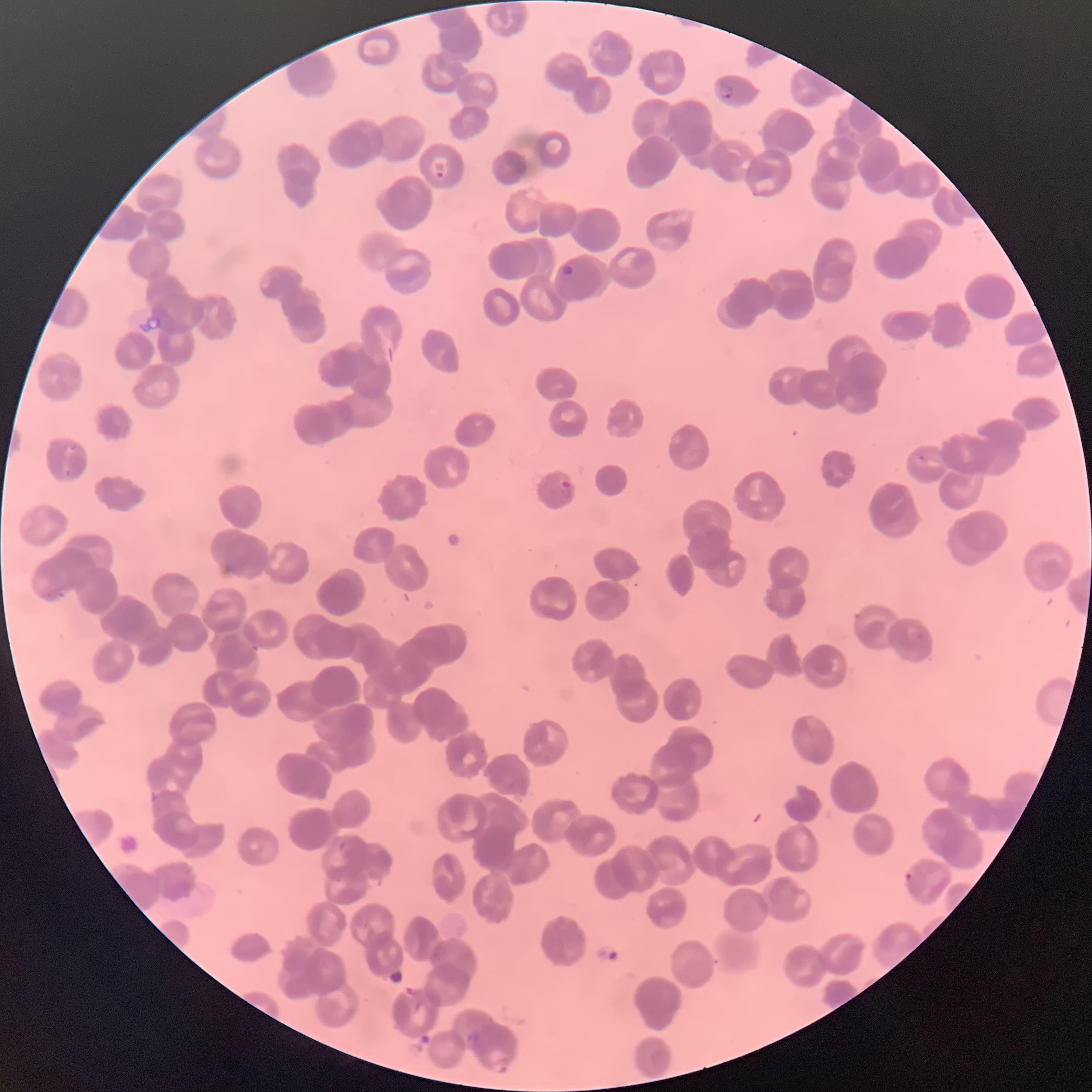
preparation: thin blood film
red_blood_cell_morphology: rouleaux formation
modality: light microscopy
plasmodium_parasite_locations: 'approximate bounding boxes as named x1/y1/x2/y2 corners in pixels: (x1=717, y1=82, x2=734, y2=100), (x1=433, y1=161, x2=446, y2=178), (x1=561, y1=264, x2=574, y2=277), (x1=917, y1=454, x2=926, y2=462), (x1=558, y1=478, x2=572, y2=498), (x1=903, y1=870, x2=914, y2=883)'
image_size: 1092×1092 pixels